Report the malaria status.
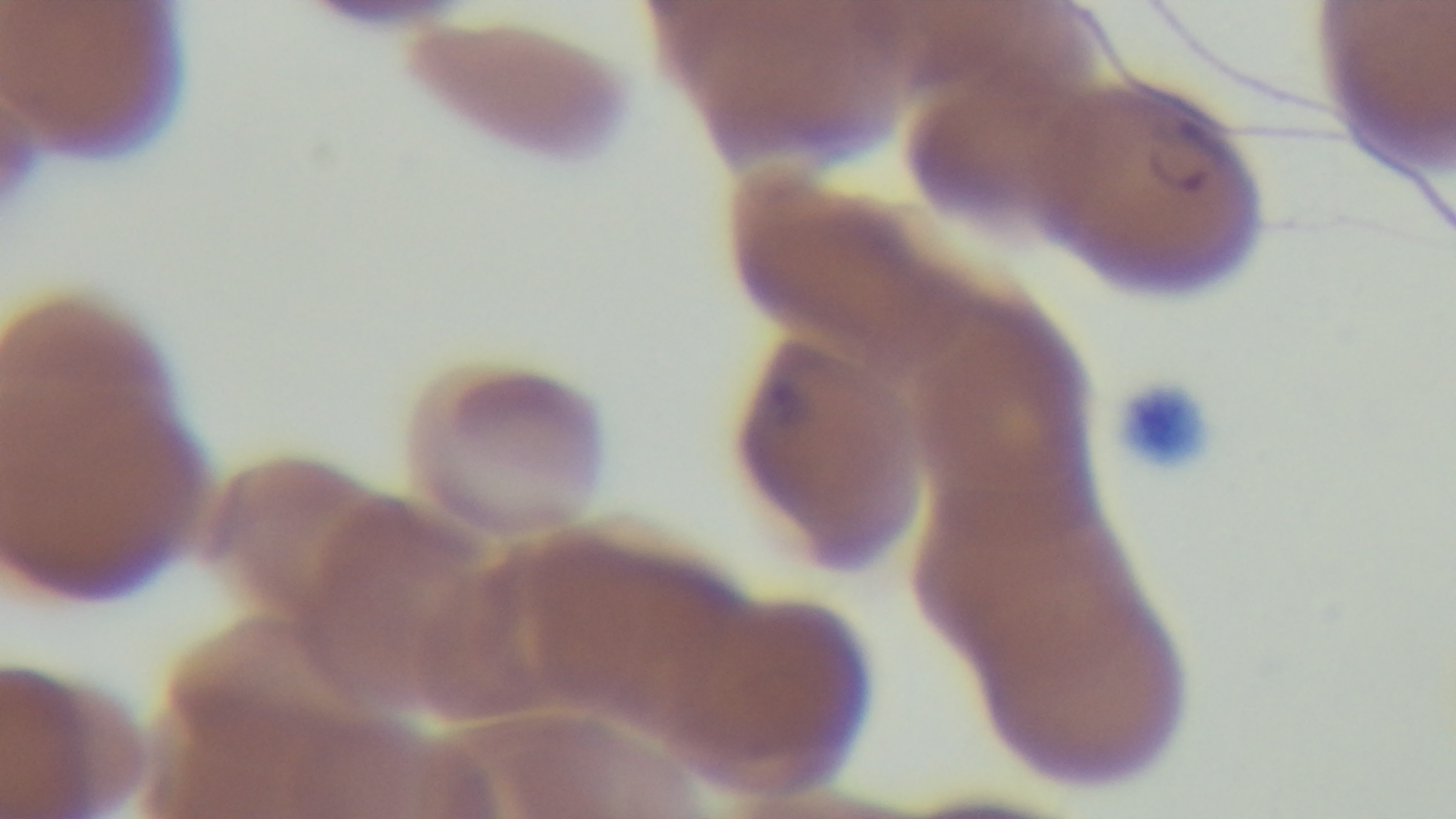

Infected.

modality: light microscopy
preparation: thin
objective: 100x oil immersion
capture: mounted 4K digital camera
stain: Giemsa
field_of_view: one from the slide